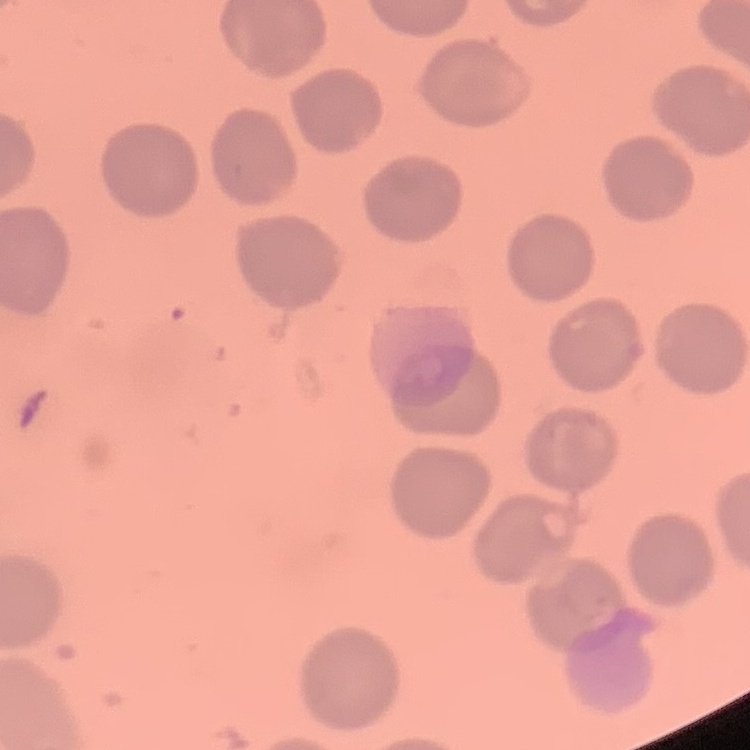

Summary:
  - Erythrocyte morphology: no rouleaux formation
  - Image type: square crop of a larger photomicrograph
  - Stain: Field's or Giemsa
  - Preparation: thin peripheral smear